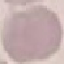

Summary:
  - Result: no malaria parasites detected
  - Preparation: thin smear
  - Image type: automatically extracted cell patch, resized to 64 × 64 pixels
  - Stain: Giemsa
  - Capture: smartphone camera at the microscope eyepiece